Locate and identify every blood parasite.
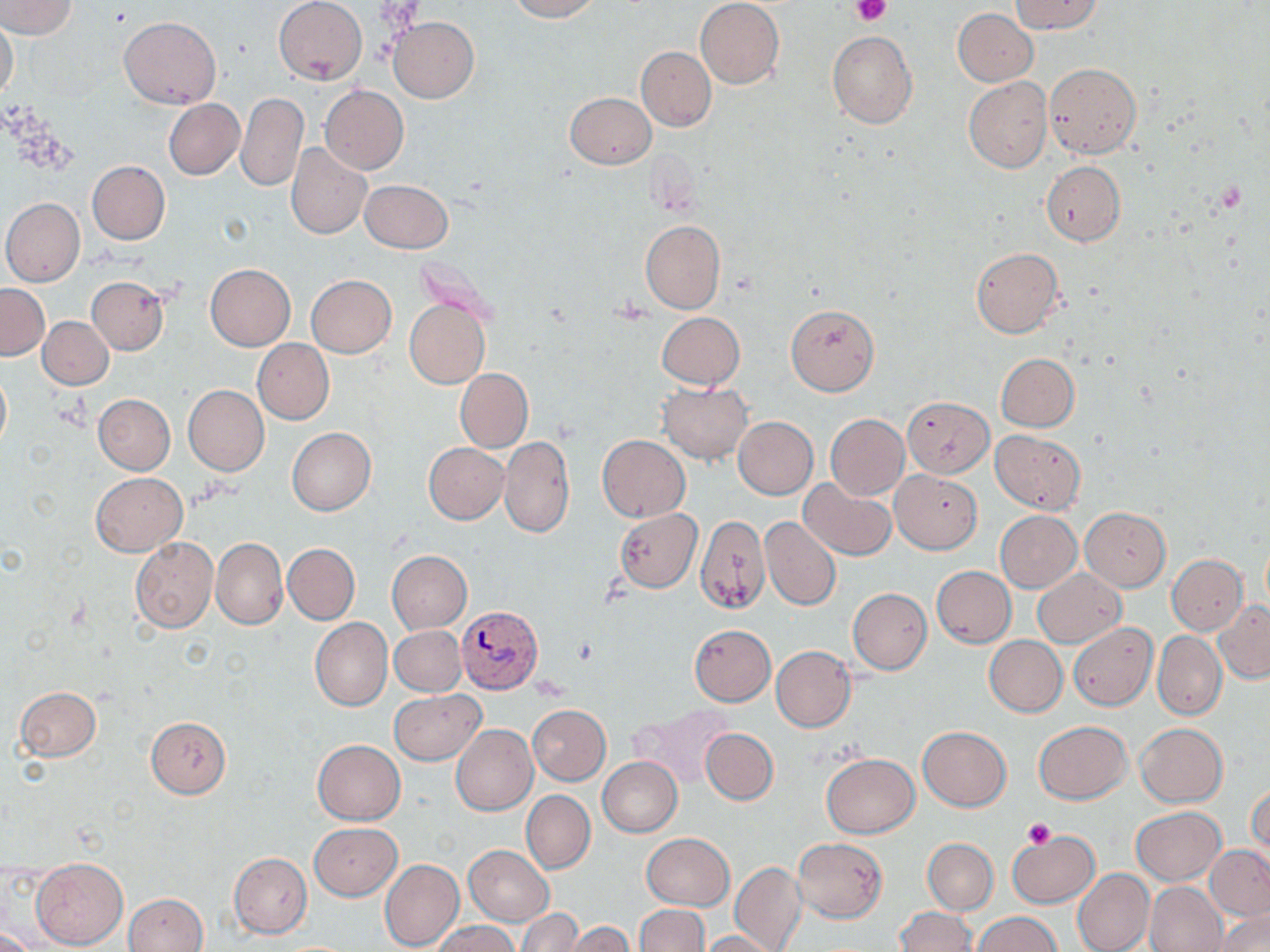
Approximate bounding boxes as [x1, y1, x2, y2] in pixels.
Plasmodium vivax-infected red blood cells: [454, 606, 541, 693].
No Plasmodium falciparum, Plasmodium ovale, Plasmodium malariae, Babesia divergens, or Trypanosoma brucei observed.

slide_level_diagnosis: Plasmodium vivax
magnification: 1000x
image_size: 1270×952 pixels
preparation: thin blood smear
platelet_locations: 'approximate bounding boxes as [x1, y1, x2, y2] in pixels: [852, 0, 889, 25], [1024, 819, 1056, 849]'
modality: light microscopy
stain: May-Grünwald-Giemsa
field_of_view: one of a larger specimen
uninfected_red_blood_cell_locations: 'approximate bounding boxes as [x1, y1, x2, y2] in pixels: [2, 0, 78, 38], [505, 0, 601, 21], [275, 1, 367, 85], [694, 1, 784, 89], [1010, 1, 1104, 35], [952, 8, 1038, 86], [119, 16, 220, 108], [0, 17, 19, 104], [388, 17, 479, 103], [827, 31, 918, 130], [637, 47, 716, 131], [1044, 63, 1141, 158], [963, 77, 1052, 172], [320, 85, 408, 175], [564, 91, 656, 168], [237, 93, 307, 193], [164, 99, 244, 180], [285, 143, 371, 238], [1041, 161, 1125, 245], [87, 162, 170, 244], [360, 179, 453, 253], [2, 198, 85, 286], [640, 221, 725, 313], [971, 247, 1064, 338], [205, 264, 295, 350], [306, 274, 396, 357], [87, 276, 170, 355], [0, 284, 49, 360], [405, 298, 490, 389], [786, 304, 879, 395], [656, 312, 744, 390], [39, 316, 113, 389], [252, 339, 334, 425], [996, 353, 1079, 432], [0, 369, 11, 452], [455, 369, 532, 452], [657, 382, 752, 465], [184, 385, 269, 475], [93, 393, 175, 474], [901, 396, 994, 477], [825, 414, 909, 500], [733, 416, 818, 499], [286, 428, 375, 515], [991, 430, 1085, 514], [499, 435, 574, 538], [597, 435, 690, 522], [423, 442, 508, 523], [890, 470, 982, 553], [91, 472, 186, 556], [799, 478, 897, 562], [1079, 507, 1171, 591], [614, 508, 702, 593], [994, 511, 1081, 592], [696, 514, 770, 615], [761, 517, 841, 611], [1261, 536, 1270, 609], [131, 537, 218, 632], [210, 537, 288, 630], [284, 543, 360, 624], [387, 550, 472, 633], [1167, 555, 1247, 635], [931, 566, 1016, 647], [1033, 568, 1127, 648], [848, 588, 932, 674], [1214, 600, 1270, 683], [310, 618, 393, 710], [1069, 622, 1158, 710], [690, 624, 776, 705], [390, 626, 465, 696], [1153, 630, 1226, 720], [984, 635, 1067, 717], [771, 645, 856, 731], [15, 686, 101, 762], [389, 689, 485, 764], [528, 704, 610, 785], [632, 705, 733, 788], [145, 716, 231, 798], [1034, 720, 1131, 804], [1135, 723, 1227, 806], [451, 724, 538, 816], [918, 726, 1011, 811], [701, 728, 778, 805], [313, 739, 405, 824], [822, 752, 918, 837], [597, 757, 682, 837], [1247, 779, 1269, 861], [522, 790, 594, 873], [1131, 806, 1225, 885], [308, 822, 401, 900], [1007, 830, 1099, 908], [640, 832, 733, 910], [793, 837, 888, 922], [923, 838, 998, 914], [464, 845, 554, 926], [1206, 845, 1270, 920], [229, 853, 312, 938], [32, 857, 128, 949], [379, 858, 463, 952], [730, 862, 806, 952], [1073, 867, 1155, 952], [1145, 881, 1227, 952], [123, 892, 208, 952], [635, 904, 709, 952], [895, 907, 977, 952], [518, 909, 582, 951], [1216, 910, 1269, 952], [975, 912, 1059, 952], [431, 921, 520, 952], [564, 922, 634, 952], [0, 926, 38, 952], [701, 930, 780, 952]'